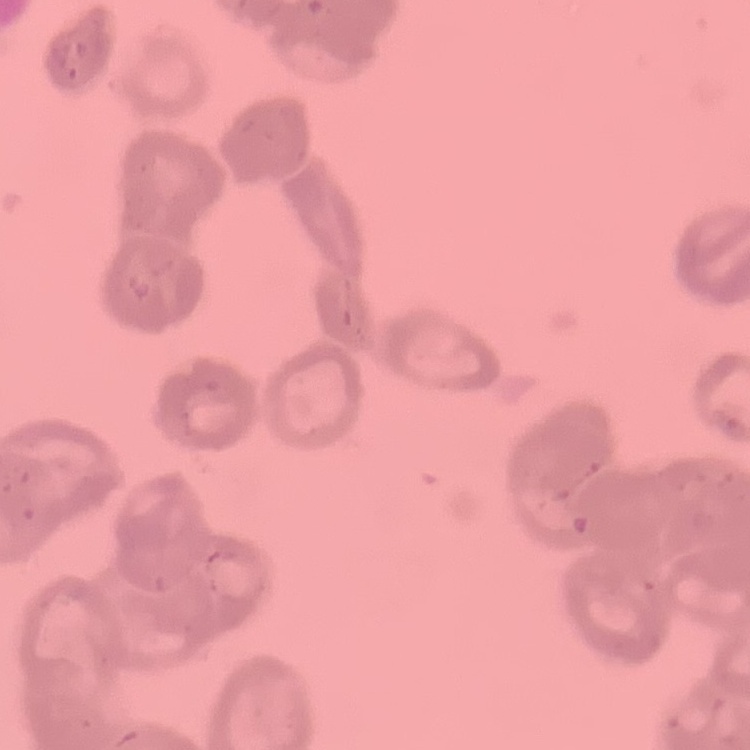

red blood cell morphology = rouleaux formation
preparation = thin blood film
stain = Field's or Giemsa
image type = square crop of a larger photomicrograph